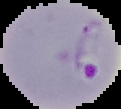
Image is 121×109 pixels. From a thin blood smear. Segmented cell region on a black background. Result: Plasmodium parasites identified.